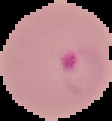

image size = 112×121 pixels
preparation = thin blood film
malaria status = parasitized
image type = segmented cell region on a black background